Name the parasite shown.
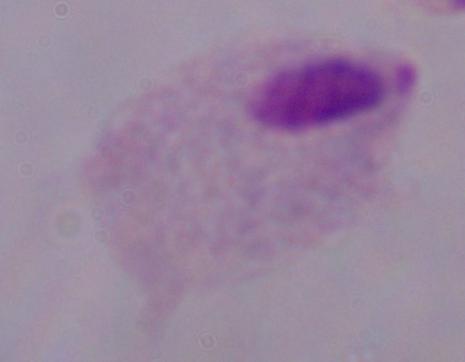
This is a trichomonad.

Summary:
  - Magnification: 1000x
  - Modality: micrograph